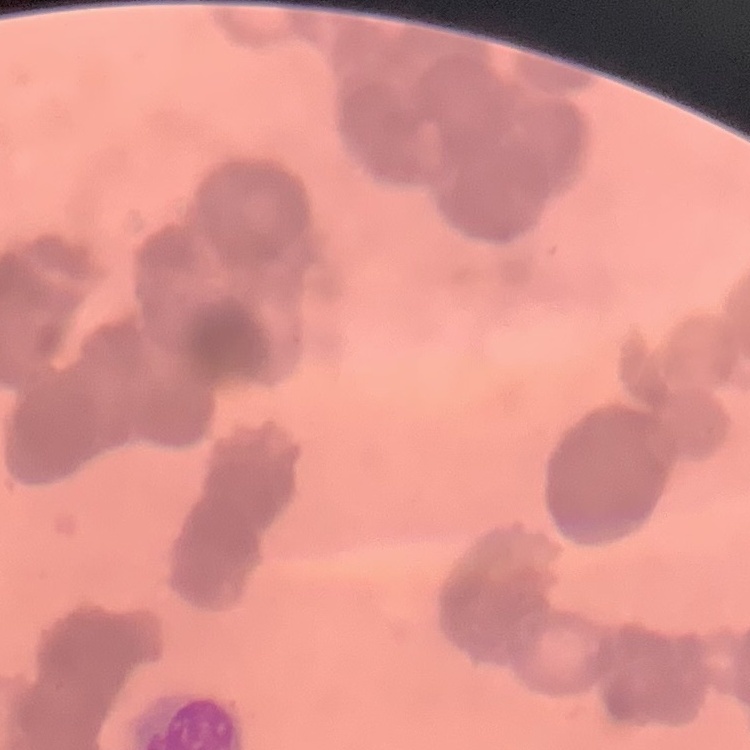
Summary:
  - Red blood cell morphology: rouleaux formation
  - Stain: Field's or Giemsa
  - Image type: square crop of a larger photomicrograph
  - Preparation: thin blood film